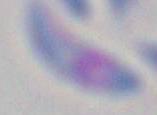
Summary:
  - Identification: Toxoplasma gondii
  - Modality: photomicrograph
  - Magnification: 1000x